Give the position of every Plasmodium parasite visible.
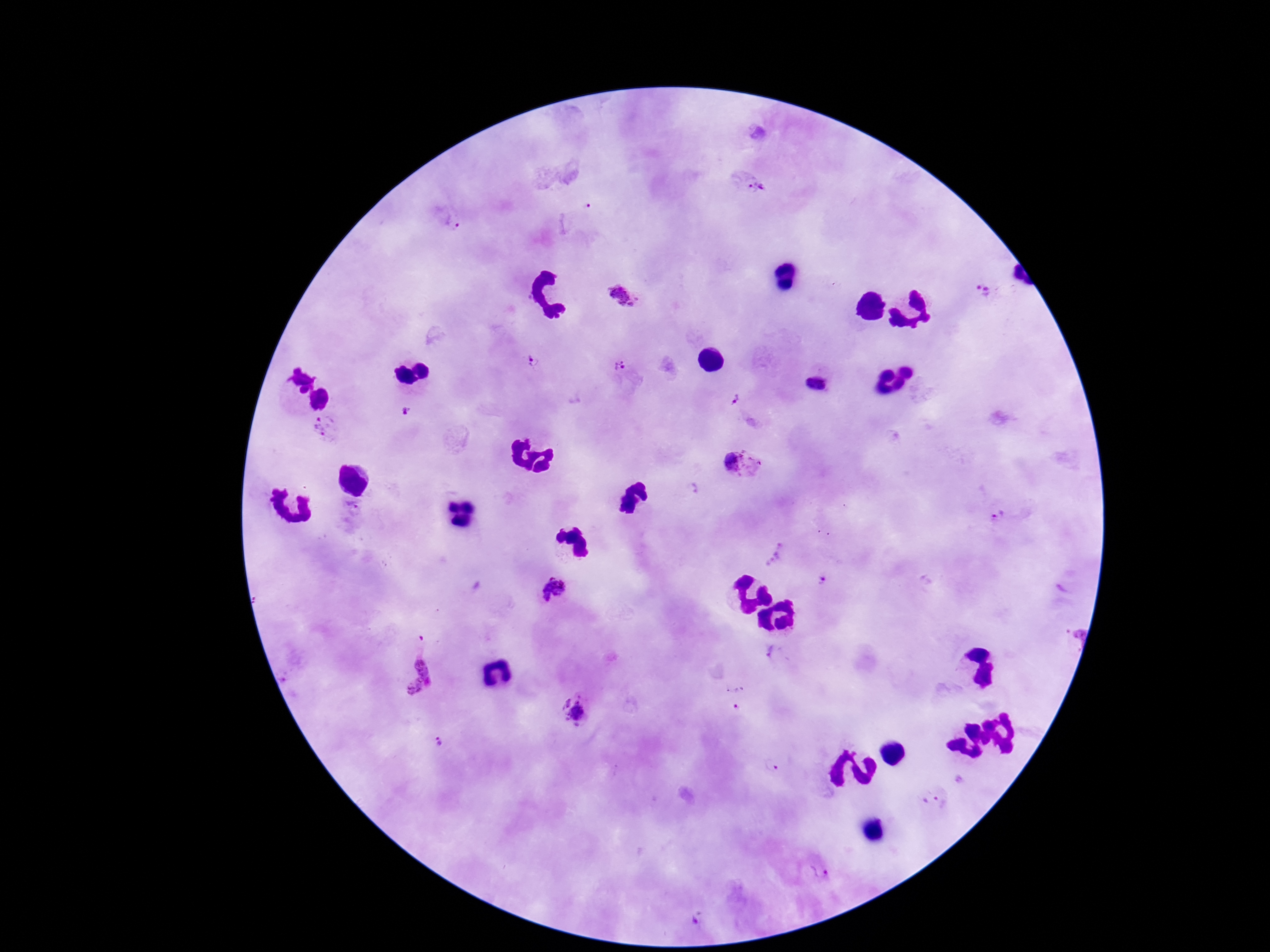

Approximate centers as (x, y) in pixels.
Plasmodium parasites: (753, 183), (585, 208), (453, 221), (985, 293), (625, 297), (534, 361), (622, 365), (735, 399), (407, 411), (325, 428), (744, 464), (693, 489), (998, 516), (775, 555), (824, 580), (1066, 587), (553, 590), (772, 652), (414, 673), (739, 705), (574, 711), (440, 743), (770, 765), (934, 801), (821, 870), (696, 918).

Thick peripheral-blood smear. Smartphone photograph taken through the microscope eyepiece. Image is 1270×952 pixels. Giemsa stain. Patient malaria status: infected. 100x magnification. Single field of view.